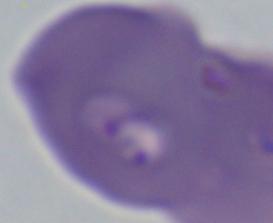

Captured at 1000x magnification. A Babesia parasite is shown. Photomicrograph.